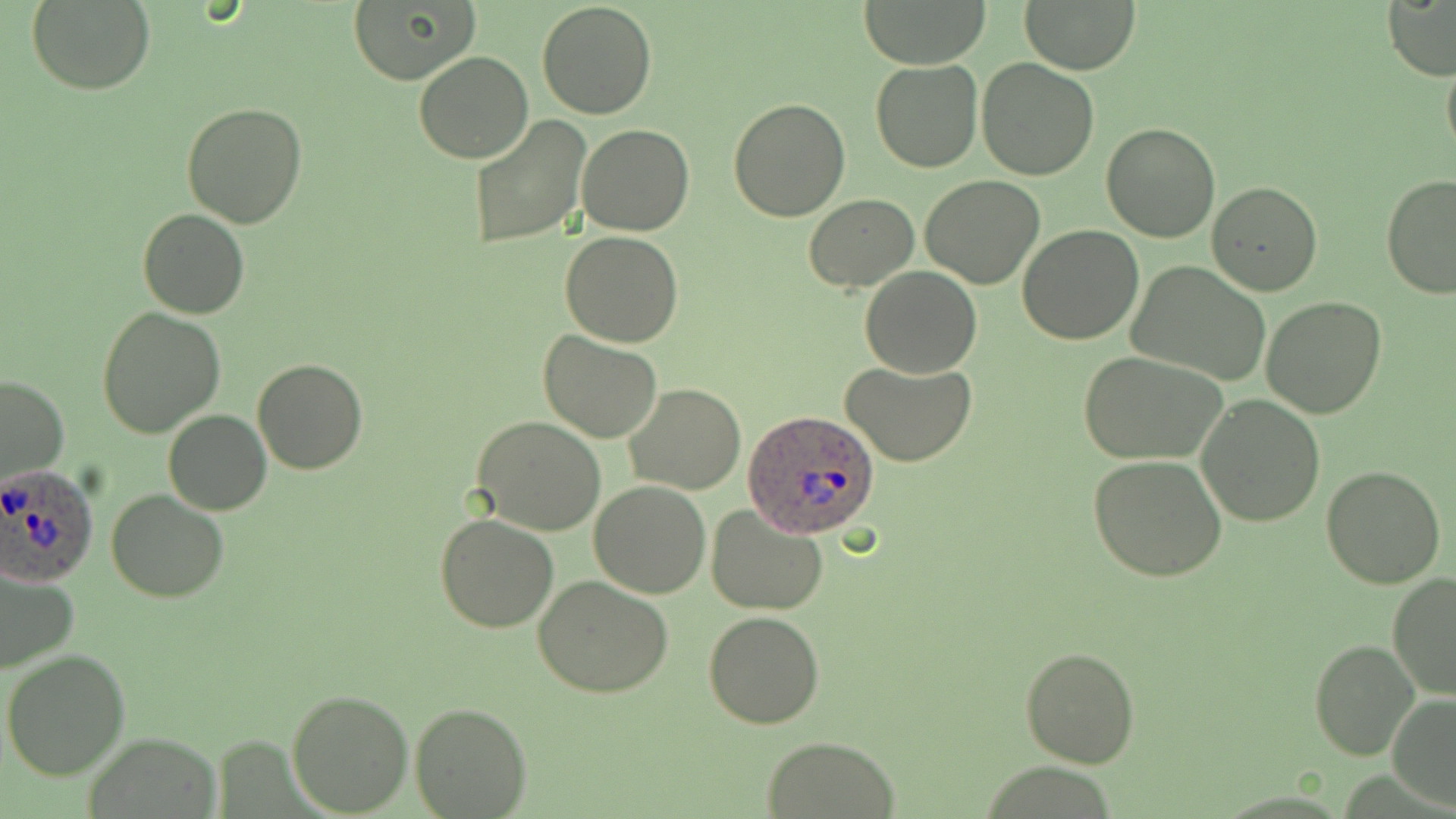
Summary:
  - Coordinate format: approximate bounding boxes as (x1, y1, x2, y2) in pixels
  - Uninfected red blood cell locations: (863, 0, 987, 68), (1017, 0, 1141, 75), (1383, 0, 1456, 81), (25, 1, 155, 94), (535, 1, 658, 119), (347, 3, 478, 84), (1441, 42, 1456, 164), (413, 51, 533, 163), (977, 58, 1098, 180), (870, 60, 982, 173), (432, 76, 574, 217), (729, 99, 850, 221), (182, 101, 307, 228), (467, 116, 592, 250), (1100, 122, 1219, 243), (577, 123, 694, 236), (1380, 174, 1456, 300), (920, 175, 1045, 289), (1208, 181, 1322, 295), (805, 194, 917, 292), (137, 208, 250, 319), (1017, 226, 1145, 346), (560, 231, 685, 347), (1128, 261, 1272, 386), (861, 268, 982, 377), (1261, 297, 1388, 419), (97, 308, 224, 438), (539, 329, 664, 442), (1079, 350, 1230, 462), (252, 358, 369, 475), (841, 360, 976, 468), (0, 374, 70, 484), (625, 382, 745, 494), (1196, 396, 1324, 526), (163, 410, 271, 516), (471, 416, 606, 535), (1087, 455, 1227, 581), (1320, 465, 1446, 589), (589, 482, 711, 599), (107, 489, 231, 602), (706, 506, 830, 615), (434, 514, 559, 633), (0, 568, 81, 675), (1388, 573, 1456, 703), (532, 575, 673, 699), (702, 610, 825, 729), (1310, 640, 1419, 760), (1020, 645, 1140, 769), (2, 647, 130, 779), (286, 687, 413, 815), (1386, 693, 1456, 812), (409, 702, 531, 817), (83, 734, 224, 818), (758, 737, 902, 818)
  - Plasmodium ovale-infected red blood cell locations: (739, 411, 882, 538), (0, 465, 99, 586)
  - Slide-level diagnosis: Plasmodium ovale
  - Field of view: one of a larger specimen
  - Preparation: thin blood film
  - Stain: May-Grünwald-Giemsa
  - Modality: light microscopy
  - Image size: 1456×819 pixels
  - Magnification: 1000x